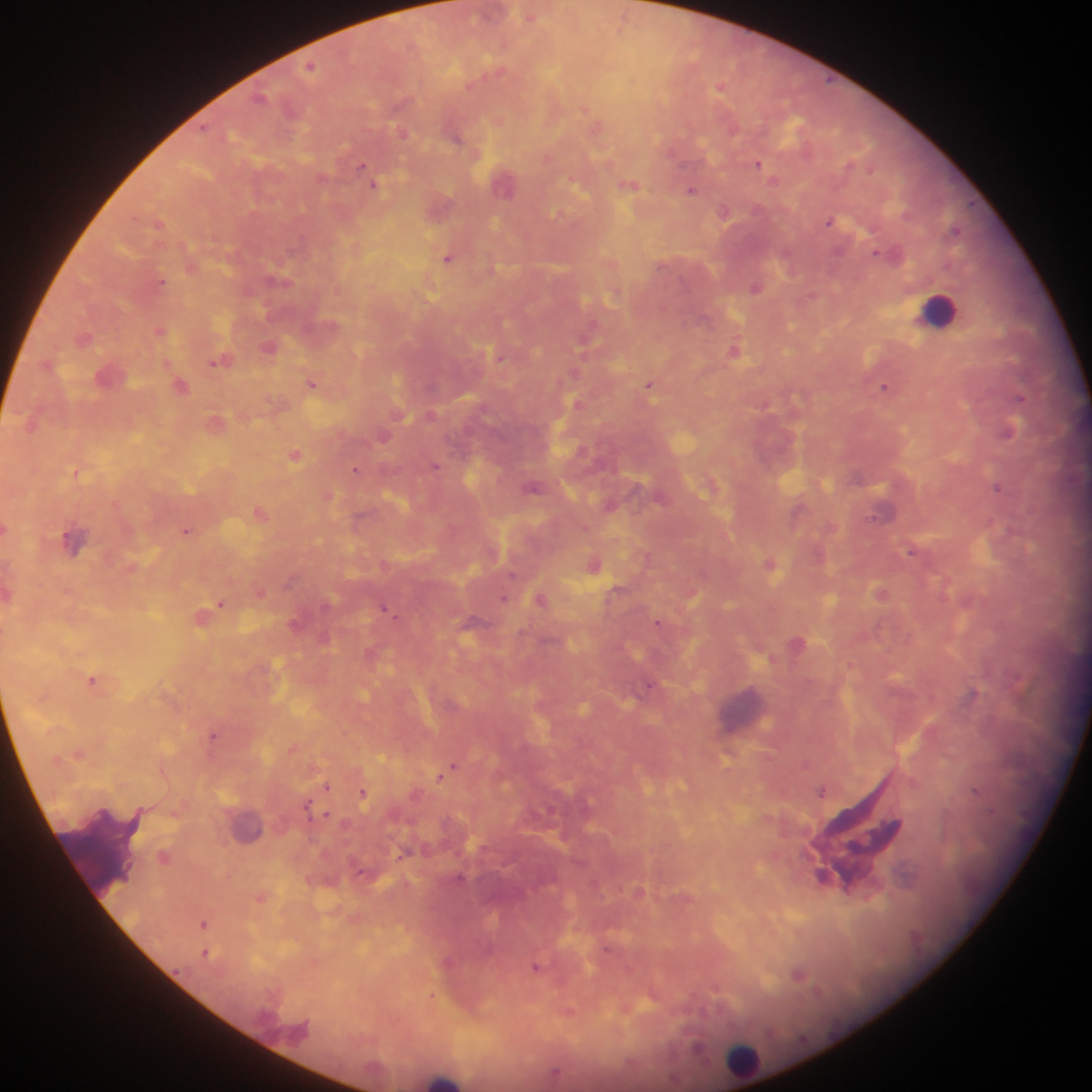

{
  "leukocyte_locations": "approximate centers as (x, y) in pixels: (938, 310), (245, 824), (105, 852), (742, 1060), (444, 1079)",
  "preparation": "thick blood film",
  "image_size": "1092×1092 pixels",
  "plasmodium_parasite_locations": "approximate centers as (x, y) in pixels: (529, 14), (311, 65), (721, 86), (597, 124), (402, 132), (455, 136), (758, 163), (364, 165), (367, 174), (505, 181), (375, 184), (630, 184), (692, 190), (439, 206), (724, 212), (830, 220), (160, 222), (877, 253), (449, 257), (279, 279), (162, 282), (756, 286), (161, 329), (83, 337), (270, 347), (735, 351), (500, 356), (220, 361), (111, 376), (313, 383), (651, 385), (181, 386), (885, 386), (1019, 397), (578, 403), (216, 422), (32, 423), (1008, 431), (384, 436), (296, 455), (436, 466), (356, 470), (76, 472), (998, 486), (534, 487), (329, 495), (611, 504), (799, 510), (260, 512), (6, 529), (187, 531), (73, 540), (912, 550), (593, 563), (771, 564), (261, 591), (882, 593), (504, 598), (541, 600), (222, 603), (386, 608), (202, 615), (659, 623), (294, 624), (325, 637), (797, 643), (372, 653), (94, 679), (652, 685), (214, 734), (293, 747), (79, 753), (453, 767), (441, 775), (327, 786), (822, 790), (362, 793), (327, 815), (403, 854), (164, 857), (639, 891), (263, 897), (205, 922), (206, 952), (448, 961), (537, 966), (798, 975), (432, 995), (569, 1012), (700, 1046), (556, 1074)",
  "field_of_view": "single",
  "country": "Ghana",
  "capture": "mobile-phone photograph through a microscope"
}